State which cell type is depicted.
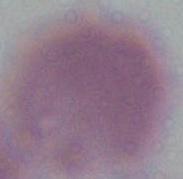
An erythrocyte.

modality = photomicrograph
magnification = 1000x